Point out malaria parasites and leukocytes.
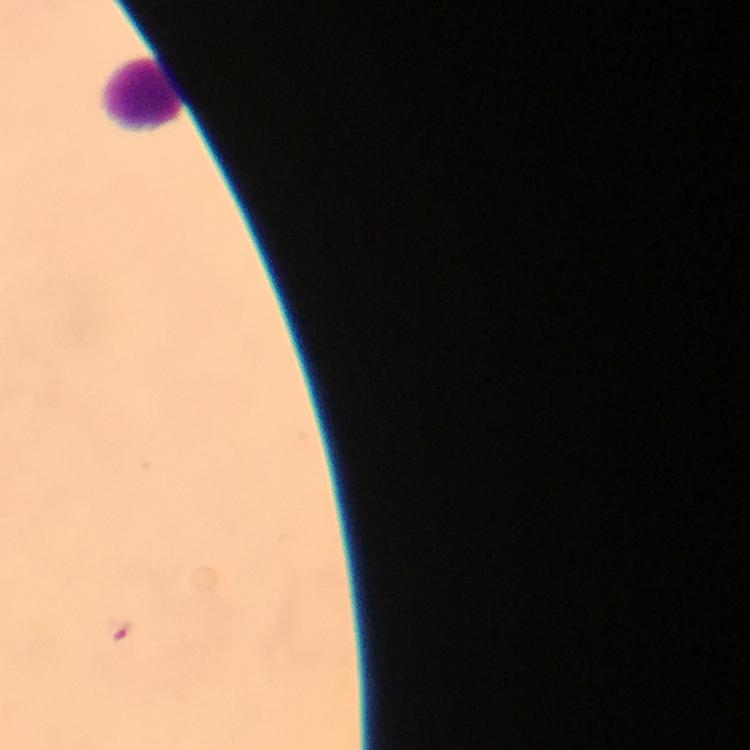

Approximate centers as {x, y} in pixels.
Malaria parasites: {117, 630}.
Leukocytes: {141, 96}.

Summary:
  - Context: from a diagnostic examination for malaria
  - Cropped from: a single field of view
  - Magnification: 100x
  - Preparation: thick blood film
  - Capture: smartphone mounted on the microscope
  - Image size: 750×750 pixels
  - Stain: Giemsa
  - Immersion oil: used